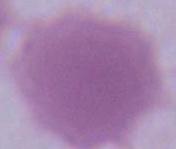

A red blood cell is shown. Captured at 1000x magnification. Micrograph.